Report the malaria status of this cell.
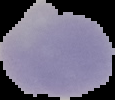

Uninfected.

image type = segmented cell region with the area outside set to black
image size = 115×100 pixels
preparation = thin blood smear